Locate every Trypanosoma brucei.
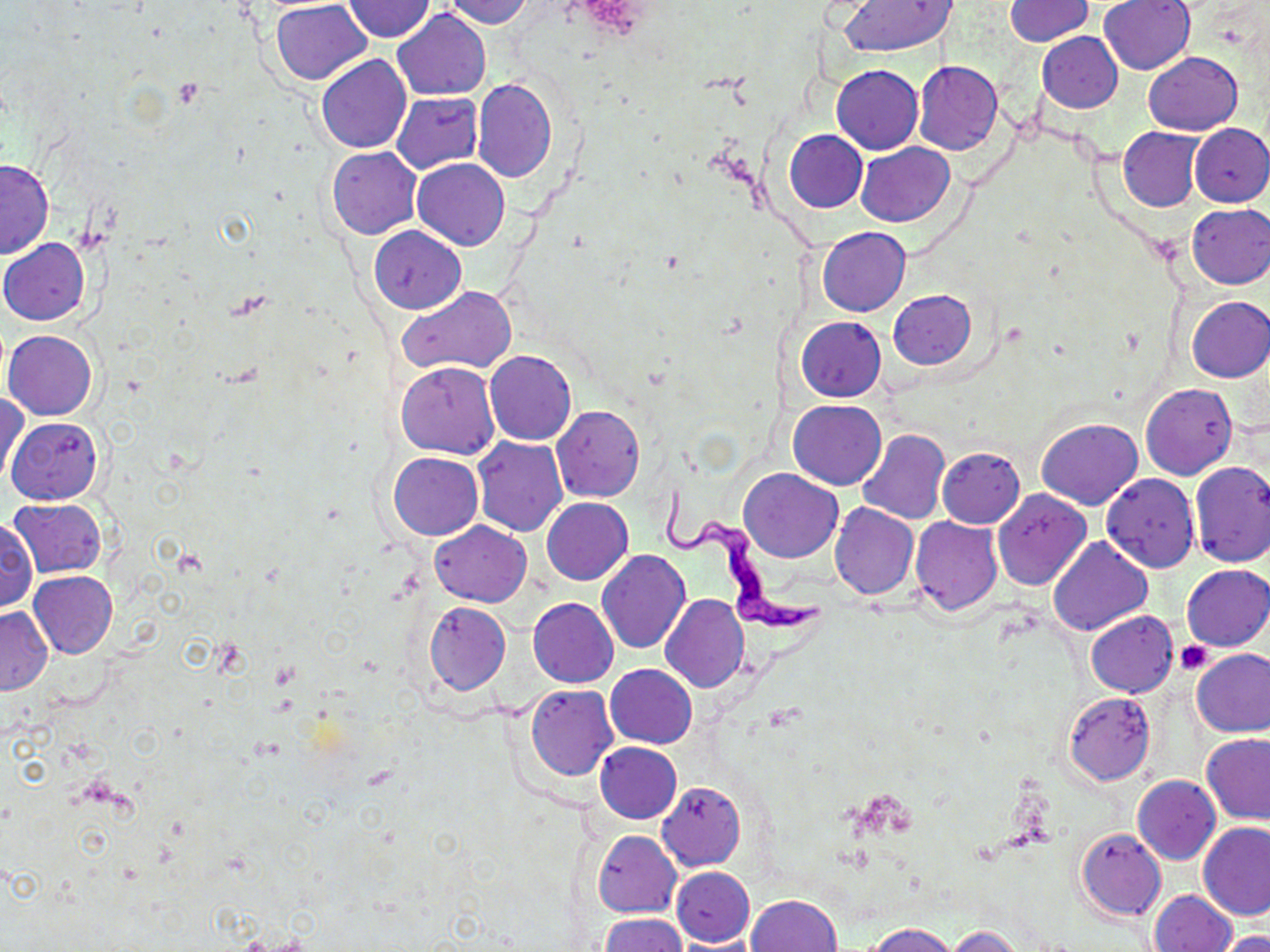
Approximate bounding boxes as (x1,y1)-(x2,y2) corner pairs in pixels.
Trypanosoma brucei: (662,480)-(826,637).

Uninfected red blood cell locations: (440,0)-(533,27), (1005,0)-(1095,45), (1099,0)-(1196,75), (270,1)-(371,85), (344,1)-(434,42), (835,1)-(958,56), (393,8)-(490,100), (1037,33)-(1122,112), (1143,51)-(1242,135), (316,55)-(410,153), (913,60)-(1002,154), (831,63)-(923,153), (472,77)-(557,183), (393,92)-(484,173), (1188,123)-(1270,207), (1118,127)-(1205,212), (785,129)-(868,213), (855,142)-(956,228), (328,146)-(422,240), (0,158)-(55,258), (412,158)-(510,250), (1186,202)-(1270,289), (369,226)-(465,313), (818,226)-(910,316), (0,237)-(89,326), (399,285)-(516,375), (889,289)-(976,370), (1186,296)-(1270,382), (796,316)-(887,402), (4,330)-(97,420), (484,349)-(576,445), (397,360)-(500,458), (1141,383)-(1237,480), (1,390)-(29,488), (788,400)-(886,489), (552,404)-(645,502), (6,416)-(102,505), (1036,418)-(1143,509), (857,428)-(950,524), (472,437)-(567,535), (936,448)-(1025,528), (390,452)-(483,540), (1189,461)-(1270,568), (739,468)-(841,562), (1101,473)-(1199,572), (992,488)-(1092,590), (541,497)-(633,584), (9,498)-(107,578), (829,503)-(919,600), (0,515)-(37,614), (910,517)-(1003,616), (430,521)-(531,606), (1048,536)-(1152,635), (597,549)-(690,653), (1182,565)-(1270,651), (29,571)-(119,659), (660,594)-(748,692), (528,597)-(618,687), (423,601)-(510,696), (0,606)-(52,695), (1085,610)-(1177,698), (1191,648)-(1270,737), (605,664)-(696,748), (526,685)-(618,780), (1063,691)-(1156,786), (1202,733)-(1270,824), (594,742)-(682,823), (1133,775)-(1221,864), (657,781)-(747,872), (1198,821)-(1270,920), (1076,827)-(1166,921), (593,831)-(682,917), (671,867)-(755,945), (1150,890)-(1236,952), (747,893)-(842,952), (599,913)-(689,952), (866,922)-(960,952), (948,926)-(1025,952), (1217,930)-(1270,952). Platelet locations: (1176,640)-(1214,674). Slide-level diagnosis: Trypanosoma brucei. Optical microscopy. Captured at 1000x magnification. May-Grünwald-Giemsa-stained preparation. Thin blood film. One field of a larger specimen. Image is 1270×952 pixels.